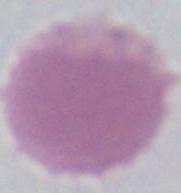
Summary:
  - Identification: red blood cell
  - Magnification: 1000x
  - Modality: micrograph